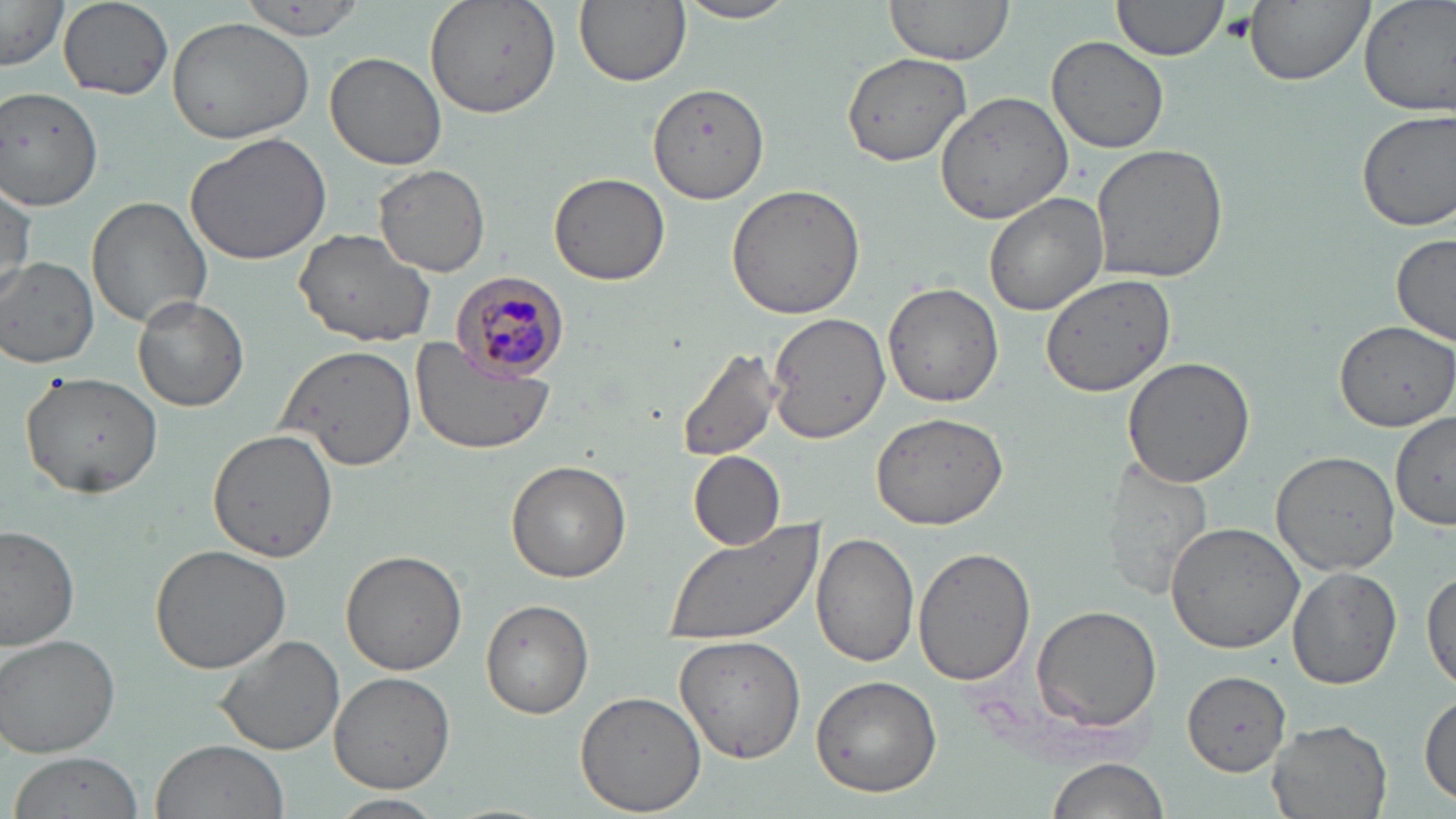

Approximate bounding boxes as (x1, y1, x2, y2) in pixels. Platelet locations: (1221, 11, 1259, 43). Uninfected red blood cell locations: (425, 0, 562, 118), (575, 0, 691, 89), (883, 0, 1015, 65), (1111, 0, 1231, 65), (1243, 0, 1373, 87), (1358, 0, 1456, 117), (58, 1, 174, 100), (675, 1, 800, 26), (0, 2, 68, 70), (237, 3, 370, 44), (166, 17, 315, 143), (1047, 35, 1170, 154), (839, 50, 974, 168), (325, 52, 449, 170), (648, 81, 771, 203), (0, 84, 104, 209), (935, 92, 1074, 222), (1355, 107, 1456, 233), (186, 131, 334, 265), (1090, 143, 1229, 284), (373, 164, 490, 276), (549, 172, 670, 285), (0, 181, 36, 299), (726, 183, 868, 321), (984, 192, 1108, 317), (86, 197, 211, 328), (295, 227, 438, 347), (1391, 233, 1456, 346), (2, 257, 99, 366), (1040, 271, 1175, 396), (883, 282, 1004, 408), (132, 293, 248, 412), (766, 313, 889, 443), (1335, 318, 1456, 430), (408, 336, 557, 456), (275, 343, 419, 471), (673, 346, 786, 465), (1122, 356, 1256, 488), (22, 371, 163, 500), (869, 410, 1011, 531), (1390, 414, 1456, 528), (208, 428, 338, 562), (1270, 450, 1401, 574), (687, 452, 785, 550), (1102, 457, 1214, 600), (506, 460, 632, 582), (1163, 521, 1305, 654), (659, 523, 824, 647), (0, 525, 79, 653), (811, 534, 920, 667), (148, 544, 292, 674), (914, 546, 1036, 687), (340, 550, 468, 675), (1287, 566, 1401, 690), (1422, 567, 1456, 696), (481, 599, 595, 718), (1032, 604, 1164, 731), (1, 633, 121, 758), (214, 635, 346, 757), (674, 636, 807, 763), (329, 671, 455, 792), (1183, 671, 1294, 775), (809, 676, 941, 798), (575, 689, 707, 815), (1419, 691, 1455, 806), (1267, 718, 1394, 819), (150, 740, 290, 819), (9, 752, 145, 819), (1044, 757, 1167, 819), (328, 793, 448, 817). Plasmodium malariae-infected red blood cell locations: (452, 272, 571, 380). Slide-level diagnosis: Plasmodium malariae. Optical microscopy. Image is 1456×819 pixels. One field of a larger specimen. May-Grünwald-Giemsa-stained preparation. Thin blood smear. 1000x magnification.